Evaluate for malaria.
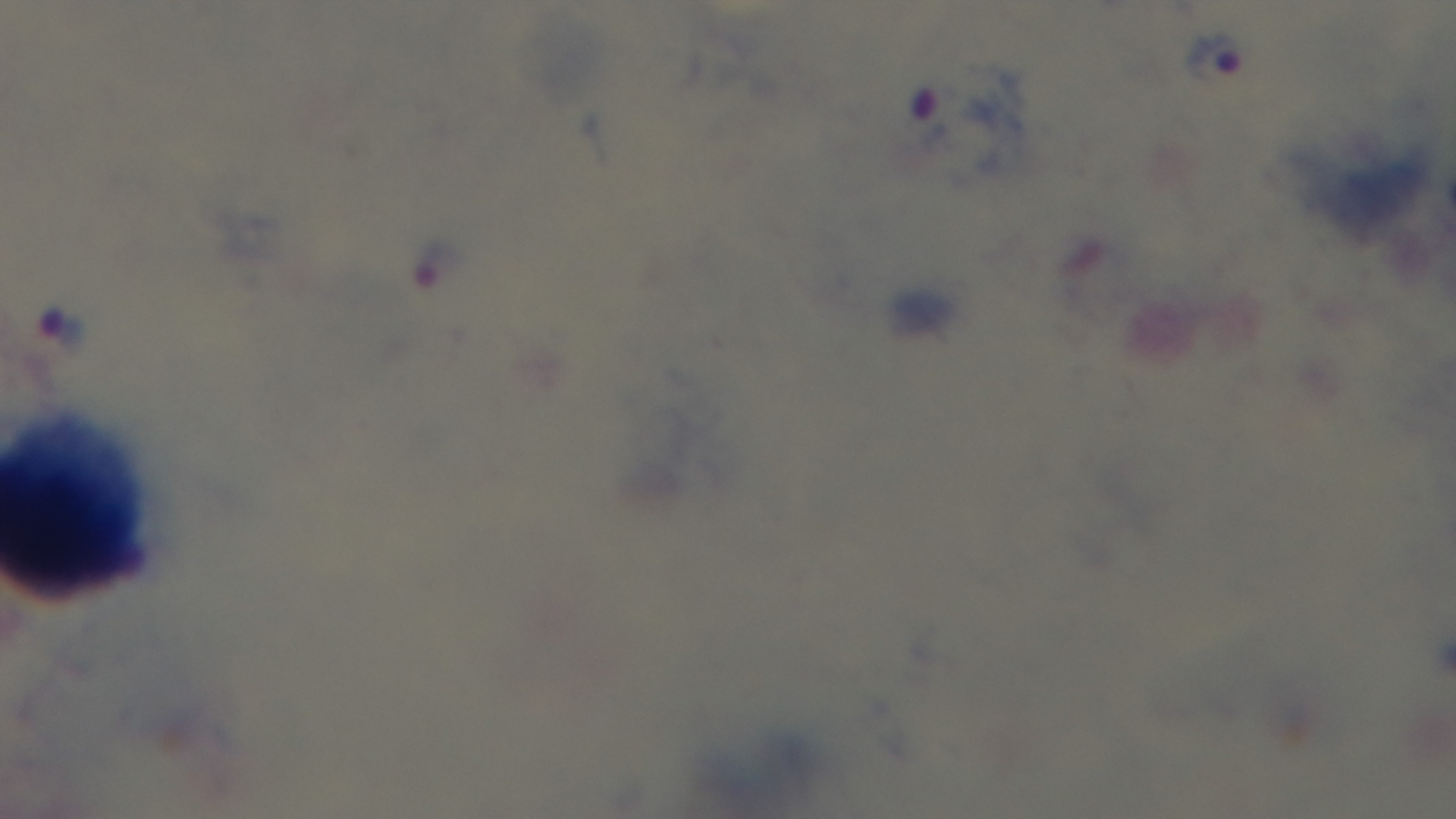

Positive.

Summary:
  - Capture: mounted 4K digital camera
  - Stain: Giemsa
  - Modality: light microscopy
  - Field of view: one from the slide
  - Objective: 100x oil immersion
  - Preparation: thick smear